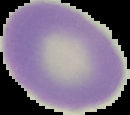
Summary:
  - Preparation: thin blood film
  - Image type: segmented cell region with the area outside set to black
  - Malaria status: uninfected
  - Image size: 130×115 pixels